Classify this cell by malaria status.
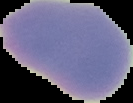

Uninfected.

Summary:
  - Image type: segmented cell region with the area outside set to black
  - Preparation: thin blood smear
  - Image size: 133×103 pixels